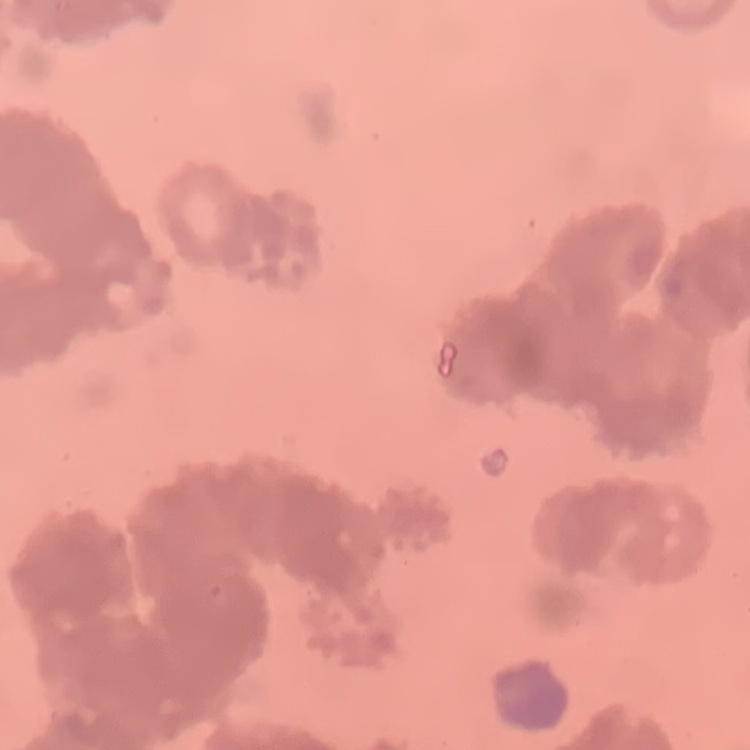

red_blood_cell_morphology: rouleaux formation
stain: Field's or Giemsa
preparation: thin blood film
image_type: square crop of a larger photomicrograph